Report the malaria status of this cell.
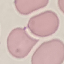

Uninfected.

Cell patch, automatically extracted from a larger field of view and resized to 64 × 64 pixels. Thin blood film. Acquired by smartphone through the microscope eyepiece. Giemsa stain.